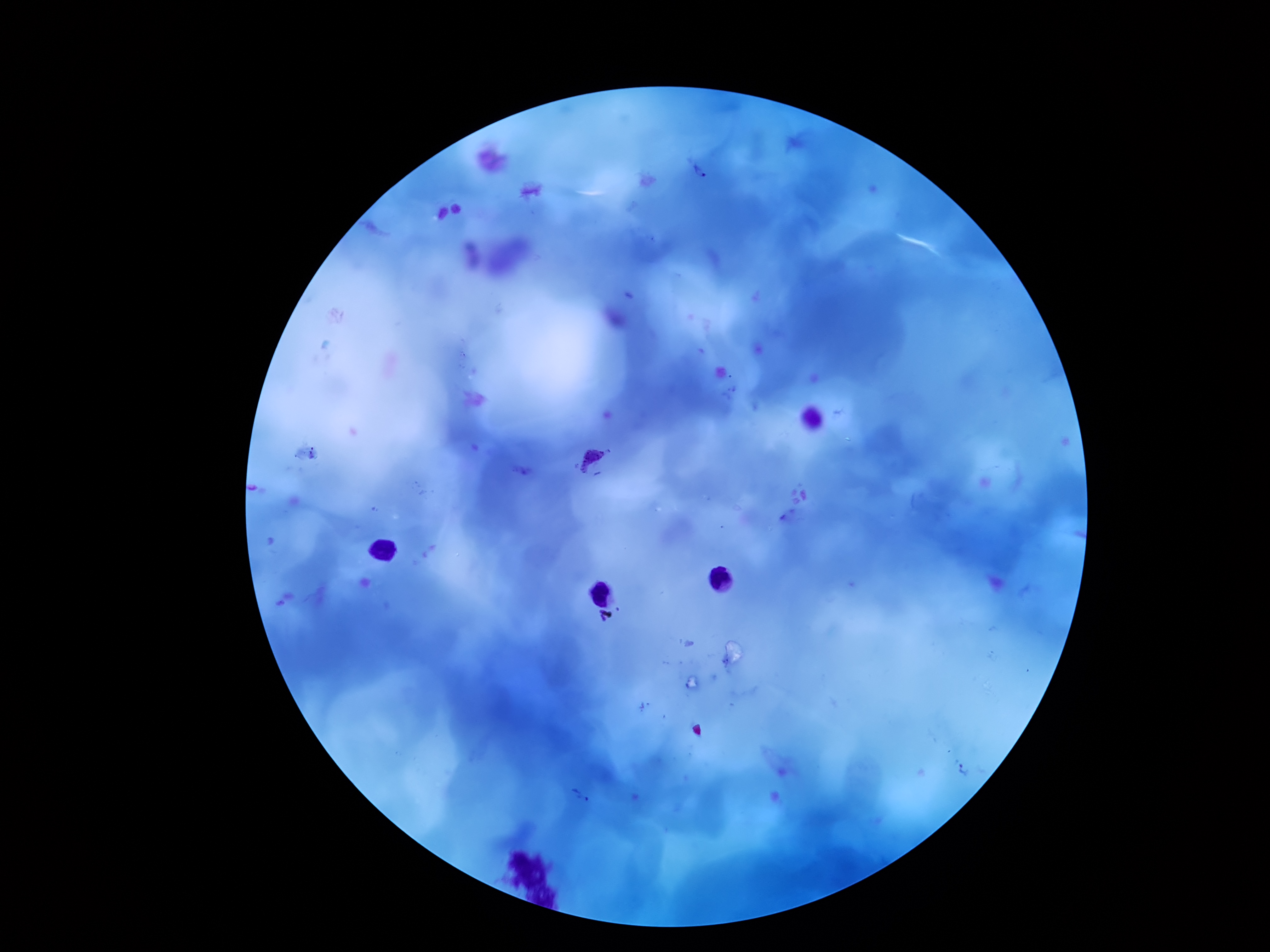
Approximate centers as (x, y) in pixels.
Summary:
  - Plasmodium parasite locations: (701, 173), (593, 462), (963, 769), (579, 796)
  - Patient malaria status: positive
  - Magnification: 100x
  - Preparation: thick peripheral-blood smear
  - Stain: Giemsa
  - Field of view: one from this slide
  - Capture: smartphone camera through the microscope eyepiece
  - Image size: 1270×952 pixels